Assess this cell for malaria.
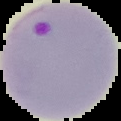
Parasitized.

Summary:
  - Image type: cell region segmented out of the field of view; surrounding area masked to black
  - Preparation: thin blood film
  - Image size: 121×121 pixels